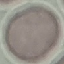
result = no malaria parasites detected
capture = smartphone through the microscope eyepiece
stain = Giemsa
image type = automatically extracted cell patch, resized to 64 × 64 pixels
preparation = thin smear